Point out each Plasmodium parasite.
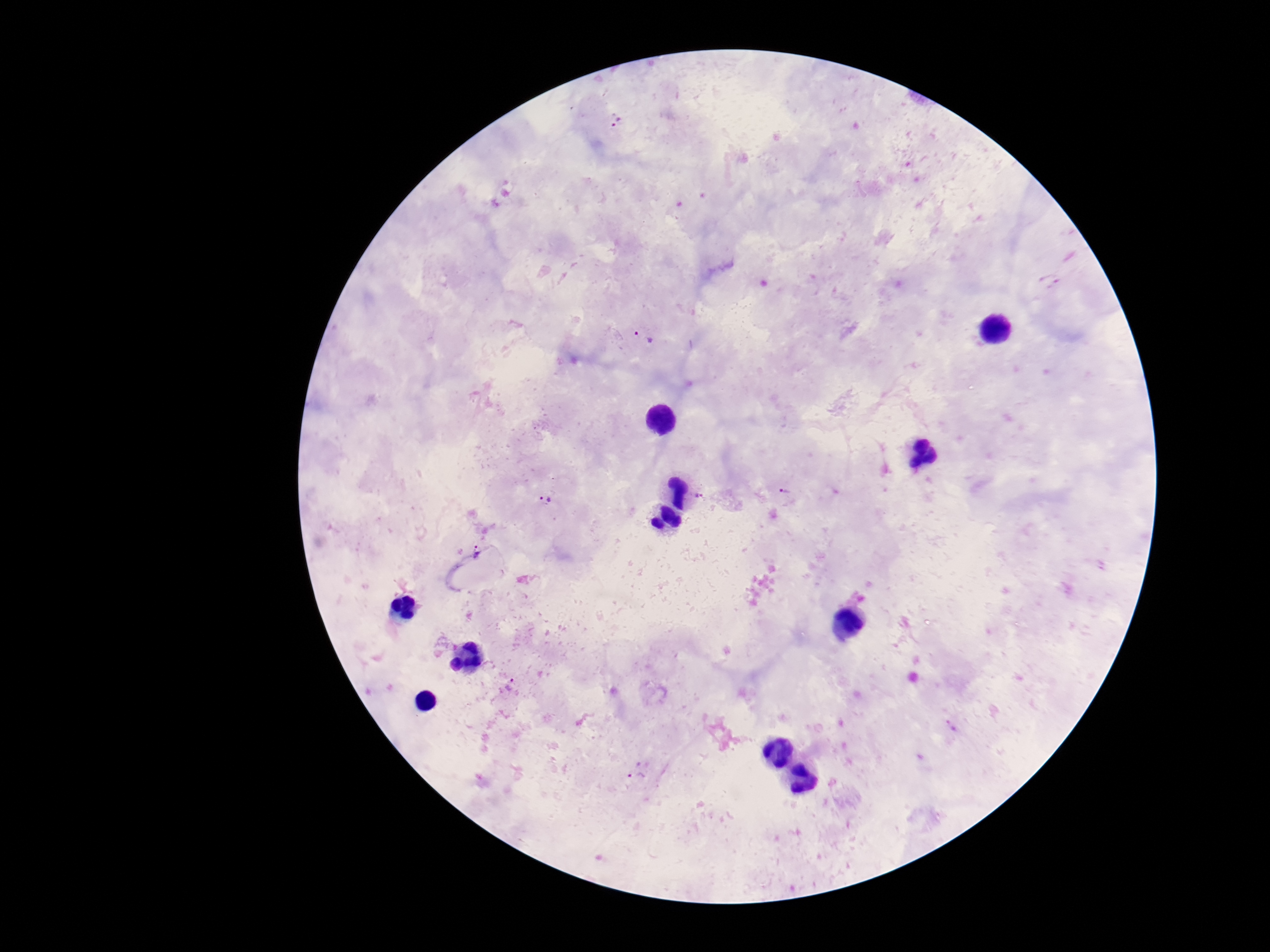
Approximate centers as [x, y] in pixels.
Plasmodium parasites: [616, 122], [644, 337], [785, 491], [699, 496], [545, 499], [477, 550], [511, 684], [636, 774].

Giemsa stain. Thick blood smear. Single field of view. Patient malaria status: positive. Image is 1270×952 pixels. Photographed through the microscope eyepiece with a smartphone camera. 100x magnification.